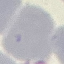

Result: no malaria parasites seen. Automatically extracted cell patch, resized to 64 × 64 pixels. Giemsa-stained preparation. Thin smear of blood. Photographed with a smartphone camera at the microscope eyepiece.